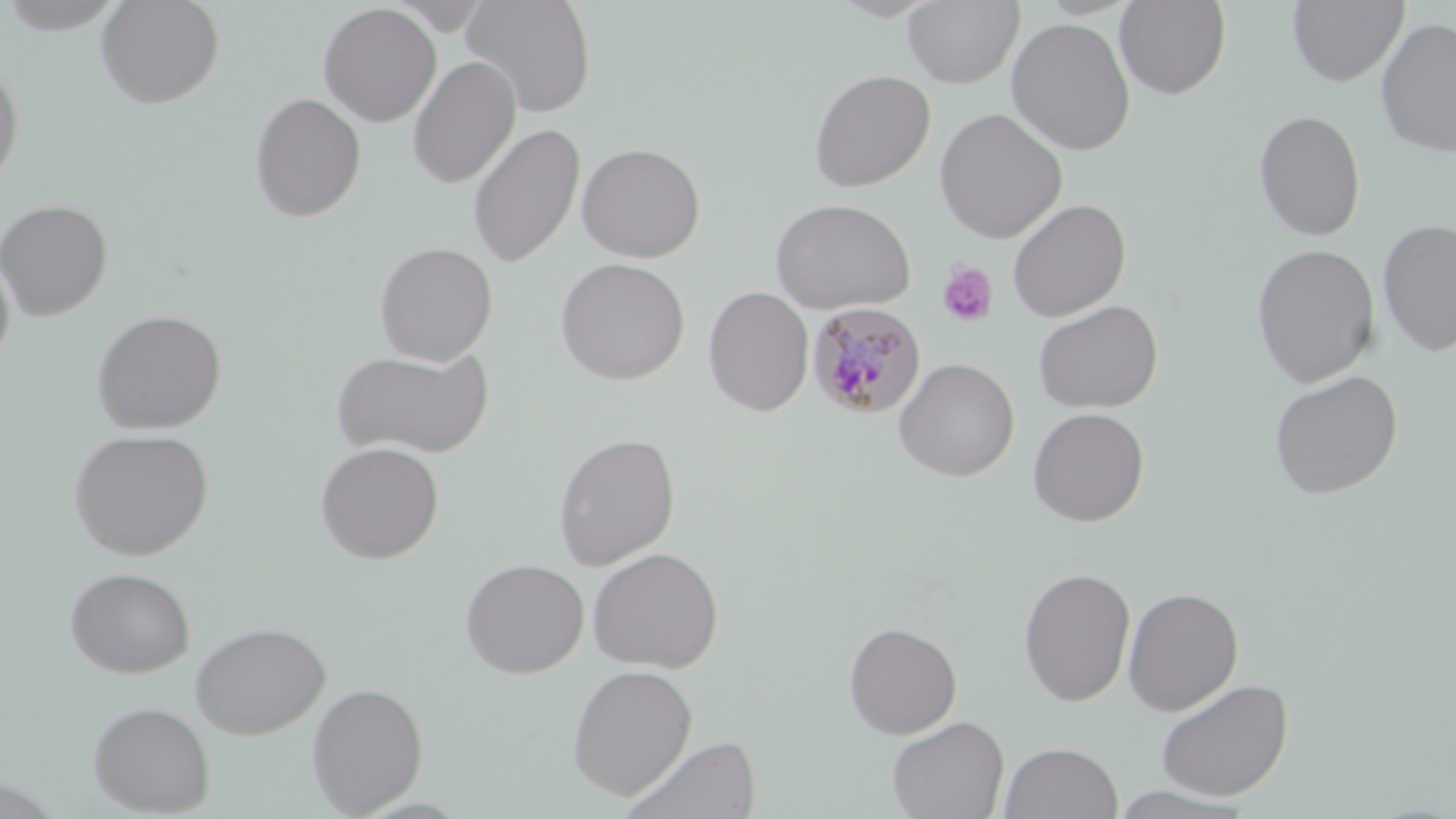

Approximate bounding boxes as (x1,y1)-(x2,y2) corner pairs in pixels. Platelet locations: (936,261)-(998,328). Plasmodium malariae-infected red blood cell locations: (806,301)-(927,419). Uninfected red blood cell locations: (96,0)-(225,109), (460,0)-(597,117), (903,0)-(1025,88), (1114,0)-(1231,99), (1288,0)-(1409,86), (0,1)-(130,35), (318,3)-(441,126), (1006,17)-(1136,156), (1375,17)-(1456,158), (407,56)-(521,188), (0,58)-(25,189), (808,69)-(935,192), (249,92)-(366,222), (934,108)-(1067,243), (1253,109)-(1366,242), (468,122)-(585,268), (577,142)-(705,262), (769,198)-(916,314), (1006,198)-(1131,321), (0,200)-(113,320), (1377,218)-(1456,357), (373,242)-(498,364), (1251,243)-(1380,387), (0,252)-(16,369), (554,258)-(690,385), (703,286)-(814,416), (1033,300)-(1163,414), (91,309)-(227,433), (332,348)-(494,459), (894,358)-(1019,481), (1269,370)-(1404,500), (1027,407)-(1149,526), (68,428)-(213,560), (553,433)-(680,570), (314,441)-(445,564), (587,547)-(723,672), (460,558)-(589,678), (64,566)-(195,678), (1018,566)-(1136,707), (1122,587)-(1244,715), (190,621)-(330,739), (843,621)-(962,739), (567,664)-(698,799), (1155,678)-(1293,800), (306,682)-(429,815), (87,700)-(215,816), (886,716)-(1009,819), (619,735)-(762,819), (999,741)-(1123,819), (1106,786)-(1257,818). Slide-level diagnosis: Plasmodium malariae. One field of a larger specimen. Thin blood smear. Image is 1456×819 pixels. Optical microscopy. May-Grünwald-Giemsa stain. 1000x magnification.